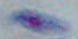

Captured at 1000x magnification. Photomicrograph. Toxoplasma gondii is seen.